Identify the blood parasite species.
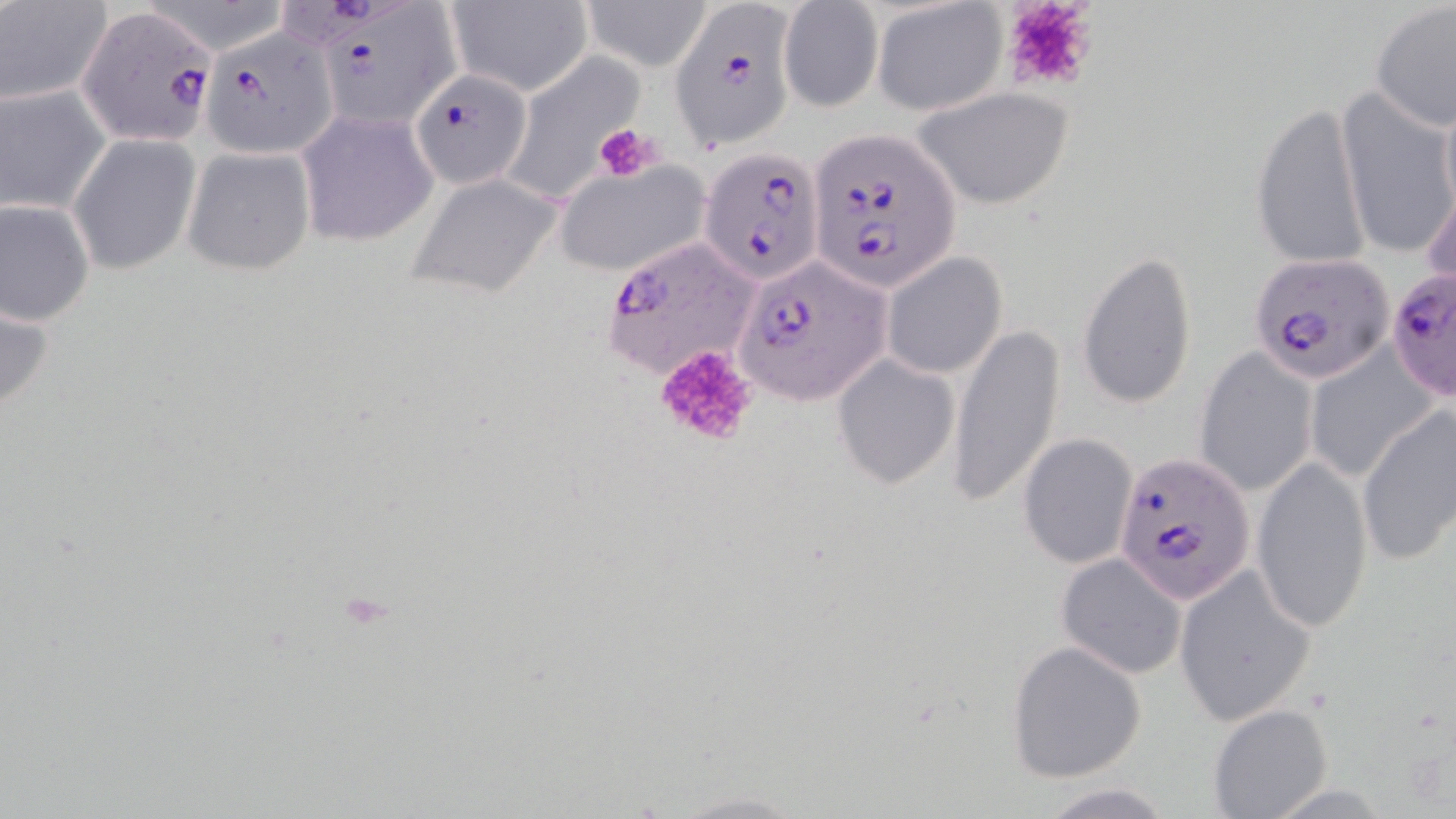

Plasmodium falciparum.

Approximate bounding boxes as [x1, y1, x2, y2] in pixels. Plasmodium falciparum-infected red blood cell locations: [314, 2, 459, 131], [76, 3, 216, 145], [669, 3, 800, 149], [202, 28, 341, 156], [409, 70, 533, 189], [805, 130, 962, 295], [699, 146, 825, 288], [598, 236, 759, 380], [735, 255, 892, 406], [1252, 255, 1395, 385], [1388, 268, 1456, 403], [1115, 455, 1257, 603]. Platelet locations: [992, 0, 1104, 97], [594, 122, 661, 183], [651, 344, 761, 450]. Uninfected red blood cell locations: [446, 0, 594, 97], [579, 0, 715, 70], [0, 1, 110, 107], [777, 2, 884, 114], [872, 2, 1008, 116], [1370, 3, 1455, 133], [505, 53, 638, 203], [1, 83, 110, 216], [912, 86, 1076, 211], [1336, 87, 1455, 257], [1248, 98, 1370, 272], [296, 108, 439, 247], [68, 135, 200, 275], [180, 147, 316, 278], [551, 161, 710, 278], [406, 170, 563, 300], [1422, 176, 1456, 304], [0, 196, 94, 326], [1078, 249, 1197, 411], [882, 253, 1008, 379], [0, 288, 57, 425], [948, 322, 1066, 508], [1303, 343, 1440, 485], [1194, 348, 1317, 498], [834, 354, 959, 490], [1356, 406, 1455, 566], [1019, 434, 1141, 570], [1250, 455, 1375, 631], [1056, 553, 1186, 680], [1174, 564, 1318, 727], [1006, 638, 1148, 781], [1208, 702, 1332, 819], [1033, 781, 1177, 818]. May-Grünwald-Giemsa stain. Optical microscopy. One field of a larger specimen. Thin blood film. Captured at 1000x magnification. Image is 1456×819 pixels.